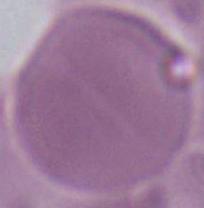

identification = erythrocyte
magnification = 1000x
modality = photomicrograph